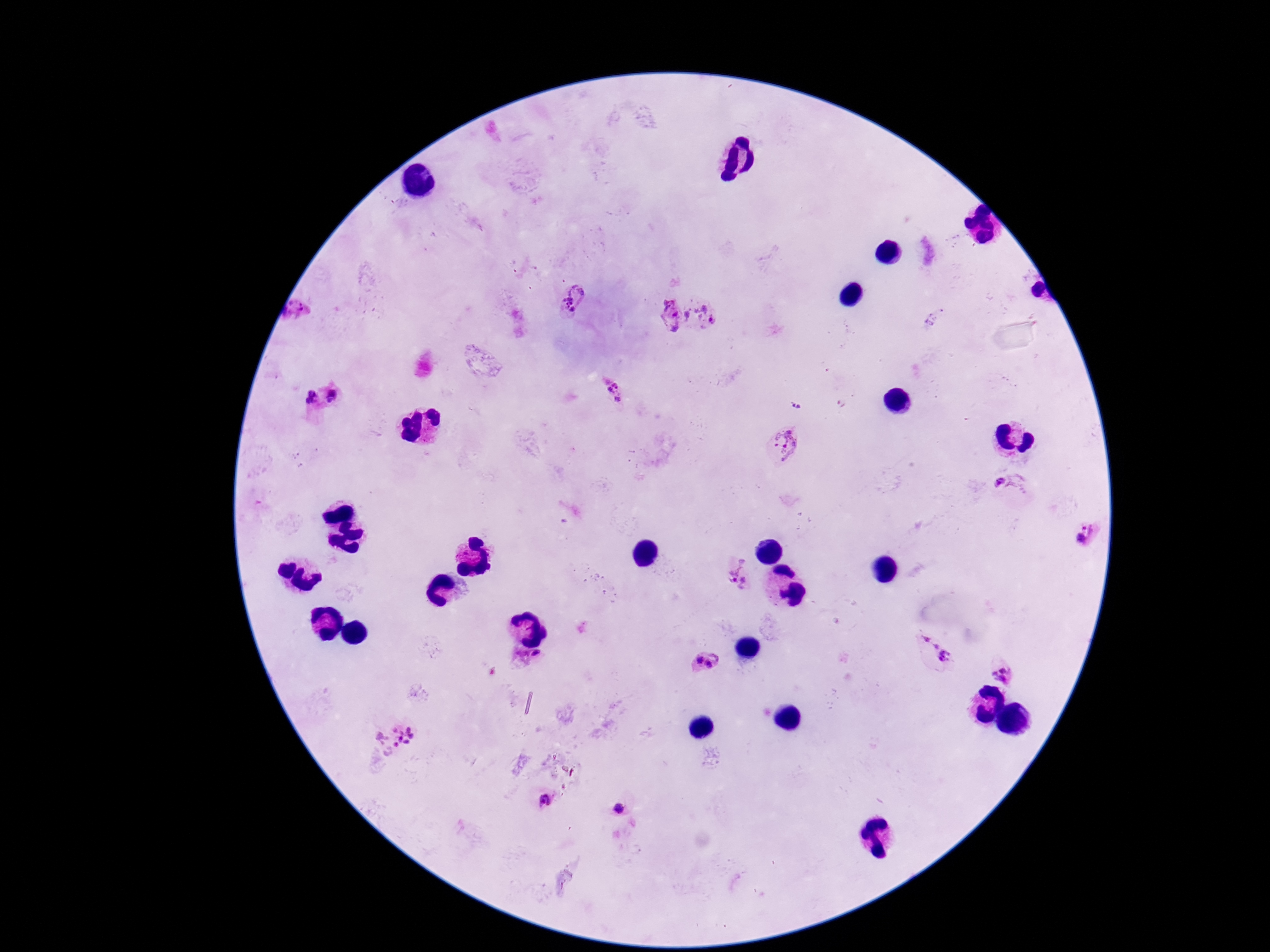

Approximate object centers, in pixels from the top-left corner. Plasmodium parasite locations: (x=574, y=298), (x=299, y=313), (x=665, y=314), (x=702, y=318), (x=937, y=318), (x=612, y=389), (x=307, y=395), (x=335, y=396), (x=797, y=406), (x=787, y=445), (x=999, y=481), (x=1018, y=482), (x=1088, y=533), (x=738, y=573), (x=939, y=644), (x=717, y=654), (x=698, y=659), (x=529, y=665), (x=709, y=665), (x=1004, y=672), (x=405, y=734), (x=380, y=747), (x=545, y=800), (x=619, y=808). Smartphone photograph taken through the microscope eyepiece. Thick peripheral-blood smear. Giemsa-stained preparation. 100x magnification. Image is 1270×952 pixels. Patient malaria status: positive. Single field of view.